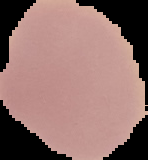
Summary:
  - Preparation: thin blood smear
  - Image type: cell region segmented out of the field of view; surrounding area masked to black
  - Result: no malaria parasites seen
  - Image size: 148×160 pixels